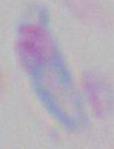

identification = Toxoplasma gondii
magnification = 1000x
modality = micrograph